Locate every uninfected red blood cell.
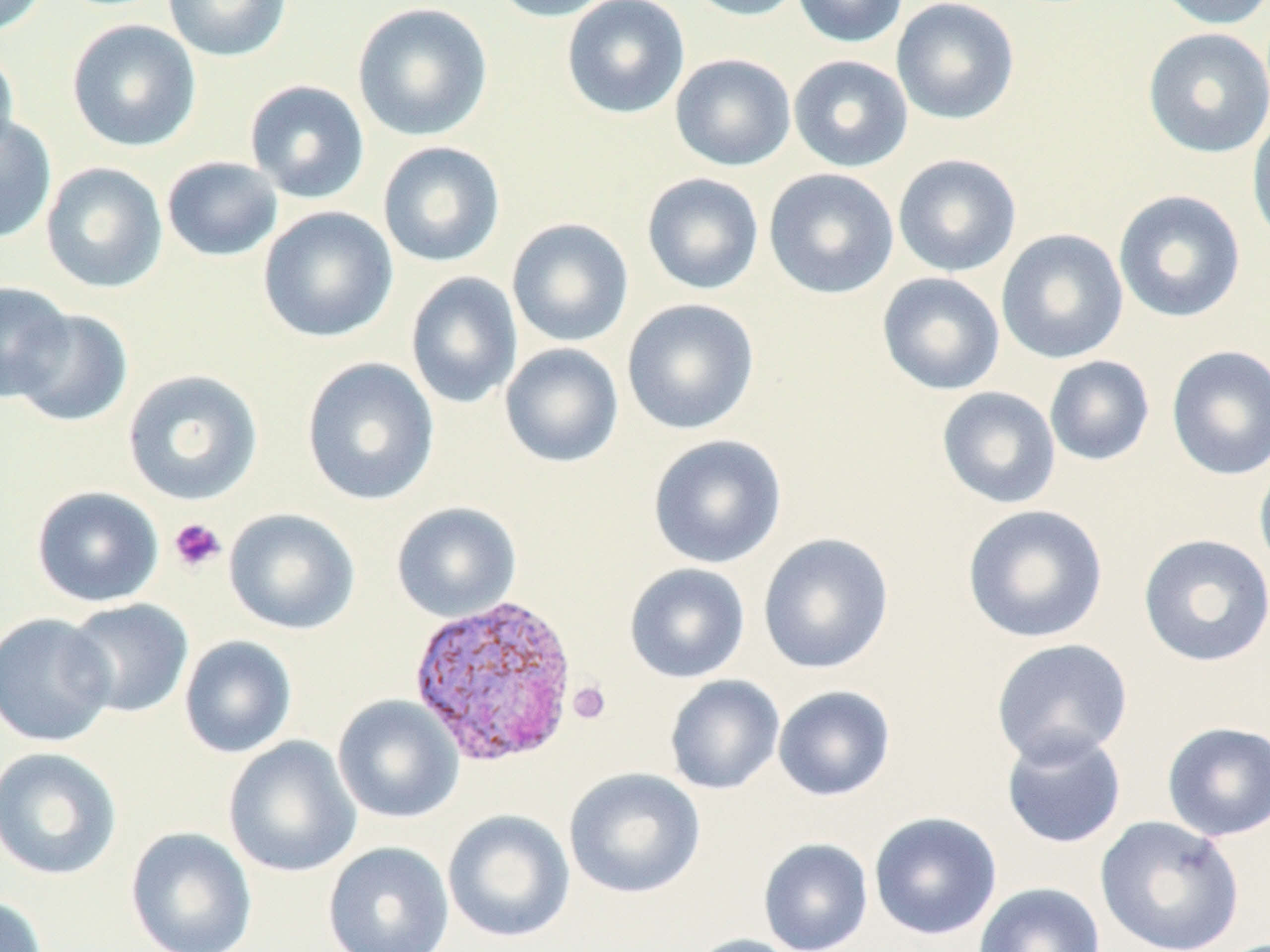

Approximate bounding boxes as (x1, y1, x2, y2) in pixels.
Uninfected red blood cells: (0, 0, 48, 36), (162, 0, 293, 62), (489, 0, 623, 23), (561, 0, 690, 119), (683, 0, 808, 21), (792, 0, 908, 48), (891, 0, 1020, 124), (1151, 0, 1270, 30), (352, 2, 493, 142), (66, 19, 201, 153), (1142, 27, 1270, 158), (0, 43, 20, 166), (670, 53, 796, 172), (789, 54, 913, 172), (243, 80, 370, 204), (1247, 109, 1270, 251), (0, 114, 57, 245), (377, 141, 506, 267), (892, 153, 1022, 277), (161, 156, 284, 262), (40, 162, 168, 294), (763, 168, 899, 299), (641, 172, 764, 295), (1113, 189, 1246, 323), (258, 206, 398, 344), (506, 217, 634, 347), (996, 228, 1128, 364), (405, 271, 523, 408), (876, 272, 1005, 396), (0, 281, 73, 402), (620, 298, 760, 436), (8, 307, 134, 427), (500, 343, 624, 468), (1166, 344, 1270, 481), (1044, 356, 1155, 466), (301, 357, 439, 505), (122, 369, 264, 506), (936, 386, 1061, 509), (648, 434, 787, 569), (1254, 455, 1270, 581), (31, 485, 165, 608), (391, 501, 522, 622), (961, 504, 1108, 644), (223, 507, 360, 635), (757, 532, 894, 674), (1137, 533, 1270, 667), (624, 562, 750, 683), (62, 598, 194, 719), (0, 612, 116, 748), (178, 635, 297, 759), (989, 638, 1134, 767), (665, 675, 785, 795), (773, 685, 896, 801), (332, 694, 464, 824), (1161, 721, 1270, 841), (1000, 728, 1127, 849), (222, 735, 362, 878), (0, 747, 123, 881), (563, 767, 706, 899), (442, 809, 575, 944), (868, 811, 1002, 941), (1095, 815, 1246, 952), (125, 826, 257, 952), (758, 838, 873, 952), (322, 841, 454, 952), (974, 882, 1106, 952), (0, 895, 49, 952), (685, 934, 805, 952).

Platelet locations: (168, 518, 227, 574), (567, 681, 611, 724). Plasmodium vivax-infected red blood cell locations: (407, 592, 579, 767). Slide-level diagnosis: Plasmodium vivax. Image is 1270×952 pixels. May-Grünwald-Giemsa stain. Thin blood smear. 1000x magnification. Optical microscopy. Single field of view.